Assess this cell for malaria.
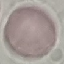

It is uninfected.

preparation: thin blood film
stain: Giemsa
image_type: automatically extracted cell patch, resized to 64 × 64 pixels
capture: smartphone camera at the microscope eyepiece